Name the cell type shown.
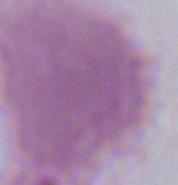

This is an erythrocyte.

Summary:
  - Magnification: 1000x
  - Modality: micrograph